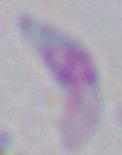
identification = Toxoplasma gondii
modality = micrograph
magnification = 1000x